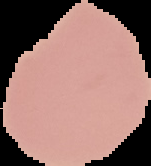
{
  "image_type": "segmented cell region with the area outside set to black",
  "preparation": "thin blood film",
  "image_size": "151×166 pixels",
  "malaria_status": "uninfected"
}